Name the blood parasite species.
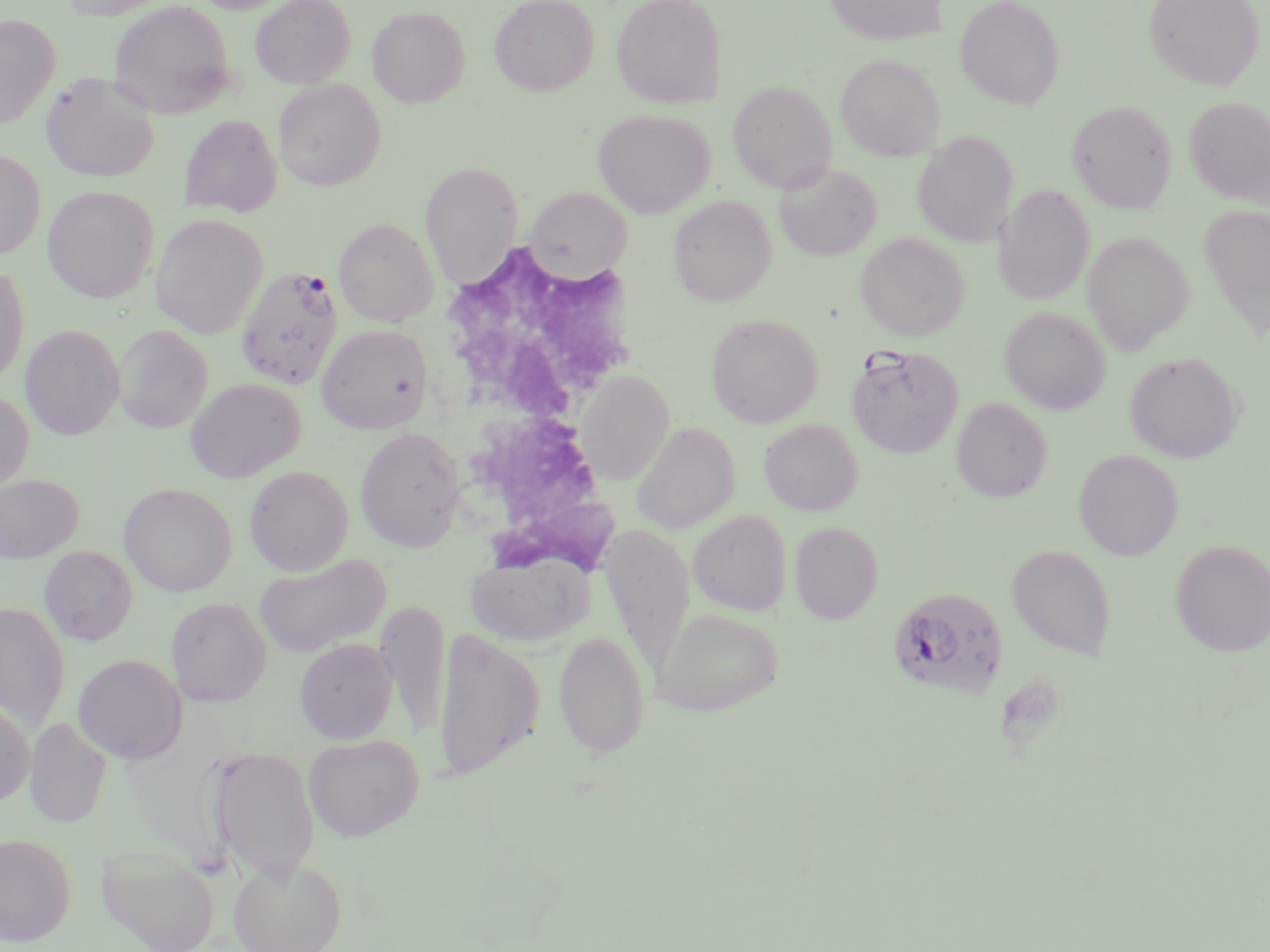
Plasmodium falciparum.

Approximate bounding boxes as [x1, y1, x2, y2] in pixels. Uninfected red blood cell locations: [60, 0, 174, 19], [250, 0, 355, 89], [489, 0, 600, 96], [611, 0, 727, 108], [823, 0, 949, 45], [955, 0, 1065, 109], [1144, 0, 1265, 91], [108, 1, 236, 119], [367, 6, 471, 108], [0, 14, 61, 130], [835, 53, 946, 160], [41, 72, 160, 182], [273, 78, 385, 190], [727, 81, 836, 193], [1184, 96, 1270, 209], [1067, 100, 1177, 214], [593, 109, 716, 217], [179, 114, 282, 217], [912, 132, 1018, 247], [0, 150, 46, 260], [421, 161, 523, 289], [775, 163, 882, 260], [994, 184, 1094, 305], [42, 185, 159, 302], [526, 189, 630, 279], [669, 196, 776, 306], [1199, 204, 1270, 341], [150, 213, 267, 338], [334, 218, 438, 327], [1083, 232, 1193, 355], [856, 233, 970, 341], [0, 264, 29, 387], [1000, 307, 1110, 414], [706, 313, 823, 427], [317, 323, 433, 433], [20, 324, 125, 439], [113, 325, 213, 433], [1125, 352, 1242, 462], [576, 372, 673, 484], [186, 377, 306, 482], [0, 389, 34, 495], [951, 397, 1052, 502], [759, 419, 862, 515], [633, 422, 739, 533], [355, 427, 466, 550], [1074, 449, 1183, 560], [245, 466, 353, 575], [0, 473, 85, 563], [119, 483, 237, 596], [688, 510, 791, 615], [789, 521, 883, 624], [1171, 539, 1270, 656], [1007, 545, 1116, 660], [39, 546, 138, 646], [465, 549, 592, 646], [254, 554, 391, 657], [165, 597, 272, 708], [377, 599, 449, 739], [0, 601, 70, 733], [654, 607, 784, 715], [434, 628, 542, 780], [554, 630, 650, 758], [294, 637, 397, 743], [73, 653, 187, 763], [0, 700, 35, 806], [25, 718, 112, 828], [303, 734, 424, 840], [207, 746, 320, 883], [0, 833, 76, 947], [97, 845, 220, 952], [229, 855, 346, 952]. White blood cell locations: [436, 242, 644, 591]. Plasmodium falciparum-infected red blood cell locations: [235, 264, 344, 390], [846, 344, 964, 459], [887, 586, 1009, 700]. Platelet locations: [996, 674, 1066, 748]. Thin blood smear. Single field of view. Optical microscopy. Image is 1270×952 pixels. May-Grünwald-Giemsa-stained preparation. Captured at 1000x magnification.